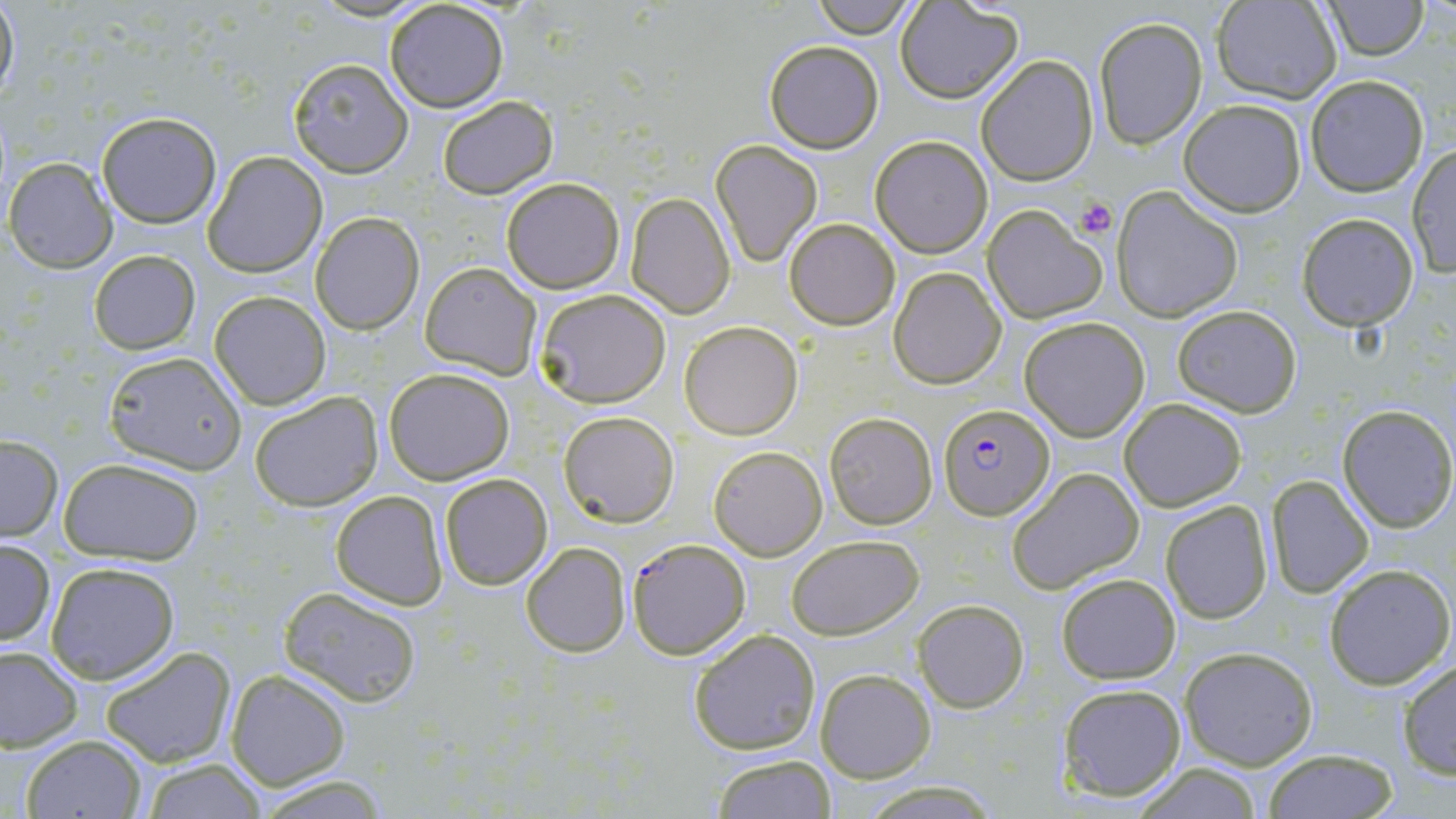

Summary:
  - Coordinate format: approximate bounding boxes as (x1,y1)-(x2,y2) corner pairs in pixels
  - Plasmodium falciparum-infected red blood cell locations (subset): (937,404)-(1054,520)
  - Uninfected red blood cell locations (subset): (0,0)-(20,104), (382,0)-(509,113), (808,0)-(917,35), (1321,0)-(1432,60), (1213,1)-(1343,103), (895,2)-(1021,103), (1094,16)-(1208,148), (764,40)-(884,153), (977,55)-(1099,185), (287,58)-(414,177), (1305,75)-(1429,196), (436,96)-(557,199), (1179,98)-(1307,217), (95,110)-(221,226), (870,135)-(992,257), (709,139)-(823,267), (1406,144)-(1455,276), (203,152)-(326,277), (5,158)-(115,272), (501,177)-(625,293), (1111,185)-(1241,321), (625,193)-(735,318), (982,204)-(1107,324), (311,211)-(425,335), (1296,212)-(1420,330), (784,218)-(900,331), (89,249)-(201,353), (420,263)-(540,379), (889,266)-(1006,389), (533,289)-(673,408), (210,292)-(331,411), (1173,305)-(1301,417), (1019,317)-(1151,440), (679,320)-(803,440), (100,349)-(247,474), (384,367)-(515,484), (250,392)-(383,511), (1119,397)-(1247,511), (1336,404)-(1455,530), (559,411)-(679,527), (824,412)-(937,530), (0,436)-(63,540), (709,445)-(827,560), (58,459)-(205,564), (1007,466)-(1145,593), (1266,474)-(1373,596), (439,475)-(552,590), (331,490)-(448,609), (1160,500)-(1273,623), (787,535)-(924,640), (0,540)-(56,647), (521,543)-(630,657), (45,561)-(180,682), (1323,563)-(1454,690), (1055,573)-(1182,684), (280,586)-(423,707), (913,600)-(1029,713), (687,629)-(822,754), (101,646)-(235,767), (1178,646)-(1319,769), (0,647)-(83,751), (1396,660)-(1455,780), (815,668)-(936,783), (226,669)-(350,789), (1056,682)-(1188,802), (18,734)-(148,818), (1263,749)-(1401,818), (711,755)-(840,818), (137,760)-(272,817), (1128,765)-(1266,818), (252,773)-(390,816)
  - Platelet locations: (1075,197)-(1117,239)
  - Slide-level diagnosis: Plasmodium falciparum
  - Magnification: 1000x
  - Image size: 1456×819 pixels
  - Stain: May-Grünwald-Giemsa
  - Field of view: one of a larger specimen
  - Preparation: thin blood film
  - Modality: light microscopy